Report the malaria status of this cell.
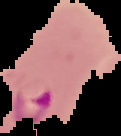

Parasitized.

Summary:
  - Preparation: thin blood smear
  - Image size: 121×136 pixels
  - Image type: segmented cell region on a black background